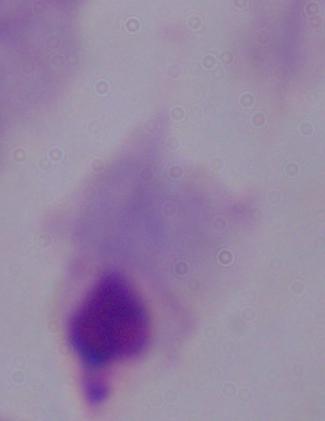

modality: micrograph
identification: trichomonad
magnification: 1000x